Describe the morphology of the red blood cells.
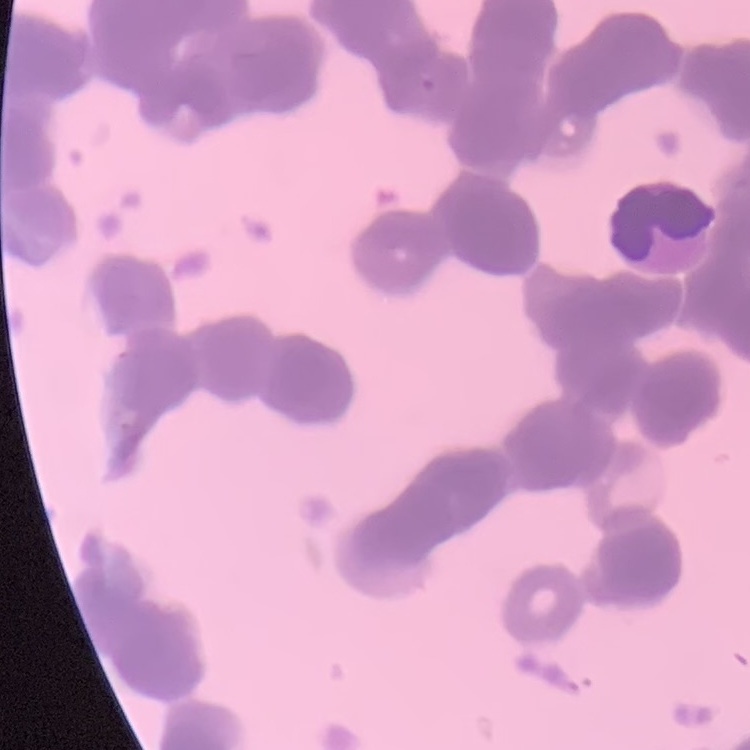
Rouleaux formation.

image type = square crop of a larger photomicrograph
stain = Field's or Giemsa
preparation = thin blood smear